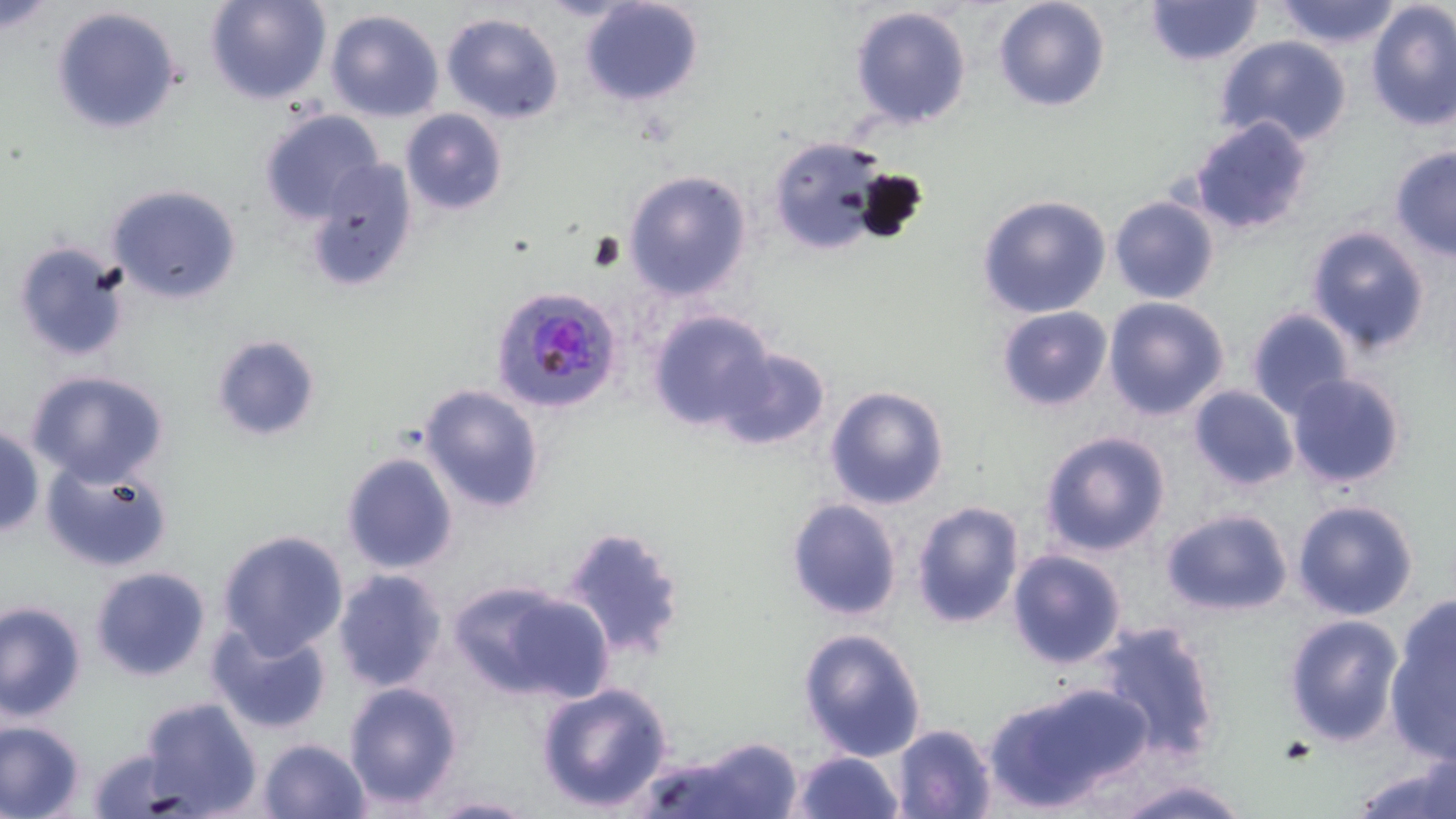

slide-level diagnosis = Plasmodium falciparum
image size = 1456×819 pixels
magnification = 1000x
modality = light microscopy
field of view = one of a larger specimen
preparation = thin blood film
uninfected red blood cell locations (subset) = approximate bounding boxes as (x1, y1, x2, y2) in pixels: (204, 0, 331, 104), (578, 0, 704, 106), (993, 0, 1110, 112), (1145, 0, 1263, 67), (1272, 0, 1404, 49), (1365, 2, 1455, 133), (50, 4, 184, 135), (849, 5, 973, 130), (325, 8, 444, 122), (441, 13, 565, 125), (1216, 37, 1352, 148), (400, 108, 508, 215), (258, 109, 385, 227), (1188, 116, 1315, 236), (766, 134, 892, 255), (1389, 145, 1456, 260), (305, 159, 420, 291), (621, 169, 754, 301), (107, 183, 243, 304), (976, 194, 1113, 319), (1109, 196, 1220, 305), (1306, 225, 1433, 353), (11, 238, 132, 364), (1102, 296, 1231, 422), (995, 305, 1113, 412), (1246, 306, 1355, 419), (647, 308, 776, 432), (210, 335, 321, 441), (711, 345, 832, 451), (24, 370, 171, 488), (1286, 373, 1406, 490), (418, 383, 548, 517), (1188, 384, 1300, 492), (824, 385, 950, 510), (0, 425, 44, 538), (1039, 430, 1170, 557), (339, 450, 459, 576), (40, 456, 175, 574), (786, 499, 904, 622), (910, 499, 1027, 629), (1292, 499, 1420, 621), (1160, 508, 1294, 617), (561, 524, 690, 661), (215, 530, 351, 659), (1006, 548, 1126, 668), (88, 565, 213, 682), (332, 569, 448, 693), (458, 581, 613, 704), (1, 600, 87, 722), (1386, 602, 1454, 759), (1283, 614, 1404, 746), (207, 619, 333, 735), (1093, 620, 1223, 765), (797, 628, 927, 762), (343, 679, 464, 808), (534, 679, 676, 814), (985, 681, 1152, 812), (139, 696, 263, 817), (0, 719, 88, 818), (891, 723, 998, 819), (675, 735, 804, 819), (257, 737, 370, 818), (86, 746, 193, 817), (789, 750, 905, 819), (1347, 753, 1456, 819), (1106, 778, 1254, 817), (421, 794, 540, 818)
stain = May-Grünwald-Giemsa
Plasmodium falciparum-infected red blood cell locations = approximate bounding boxes as (x1, y1, x2, y2) in pixels: (491, 284, 623, 416)